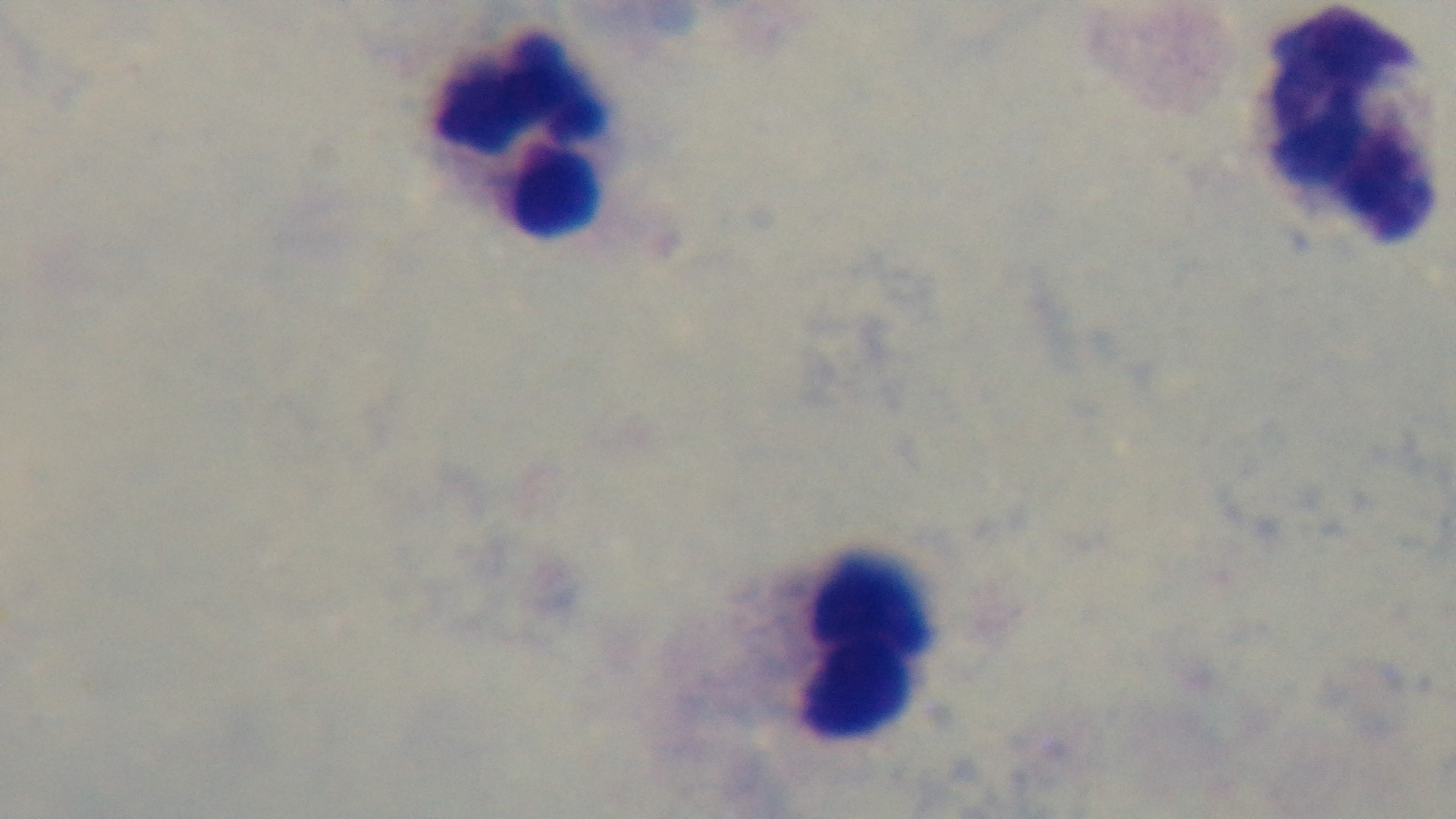

Summary:
  - Malaria status: negative
  - Objective: 100x oil immersion
  - Field of view: one from the slide
  - Capture: mounted 4K digital camera
  - Modality: light microscopy
  - Stain: Giemsa
  - Preparation: thick blood film